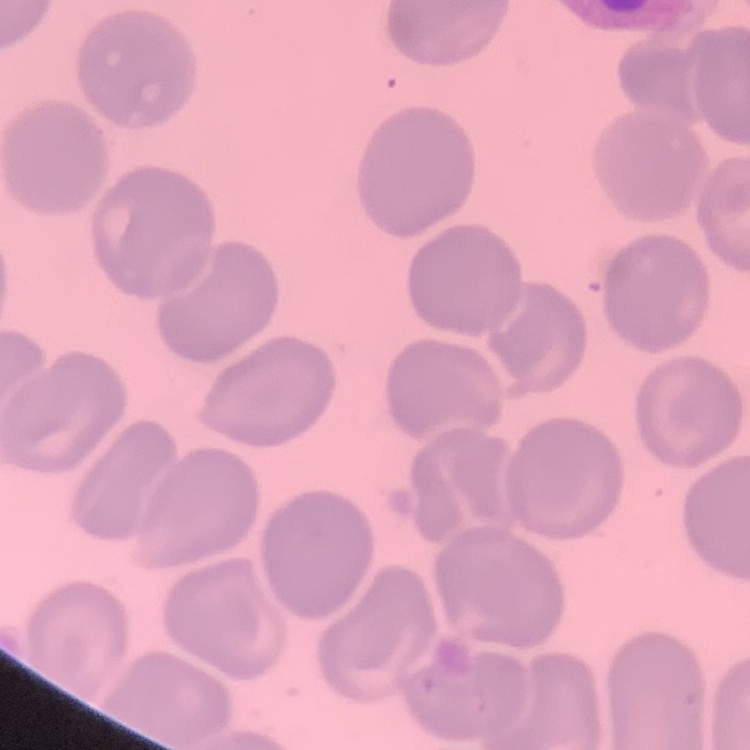

Summary:
  - Erythrocyte morphology: no rouleaux formation
  - Preparation: thin blood smear
  - Stain: Field's or Giemsa
  - Image type: square crop of a larger photomicrograph